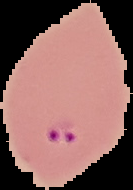

Summary:
  - Image size: 133×190 pixels
  - Result: Plasmodium parasites identified
  - Preparation: thin blood film
  - Image type: segmented cell region on a black background